Classify this cell by malaria status.
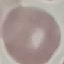

Uninfected.

Giemsa-stained preparation. Automatically extracted cell patch, resized to 64 × 64 pixels. Photographed with a smartphone camera at the microscope eyepiece. Thin smear of blood.